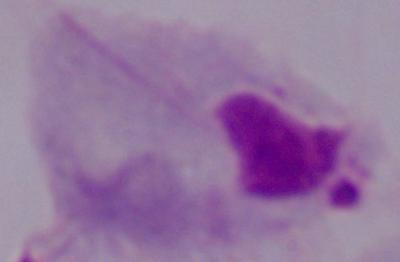

Summary:
  - Magnification: 1000x
  - Modality: photomicrograph
  - Identification: trichomonad